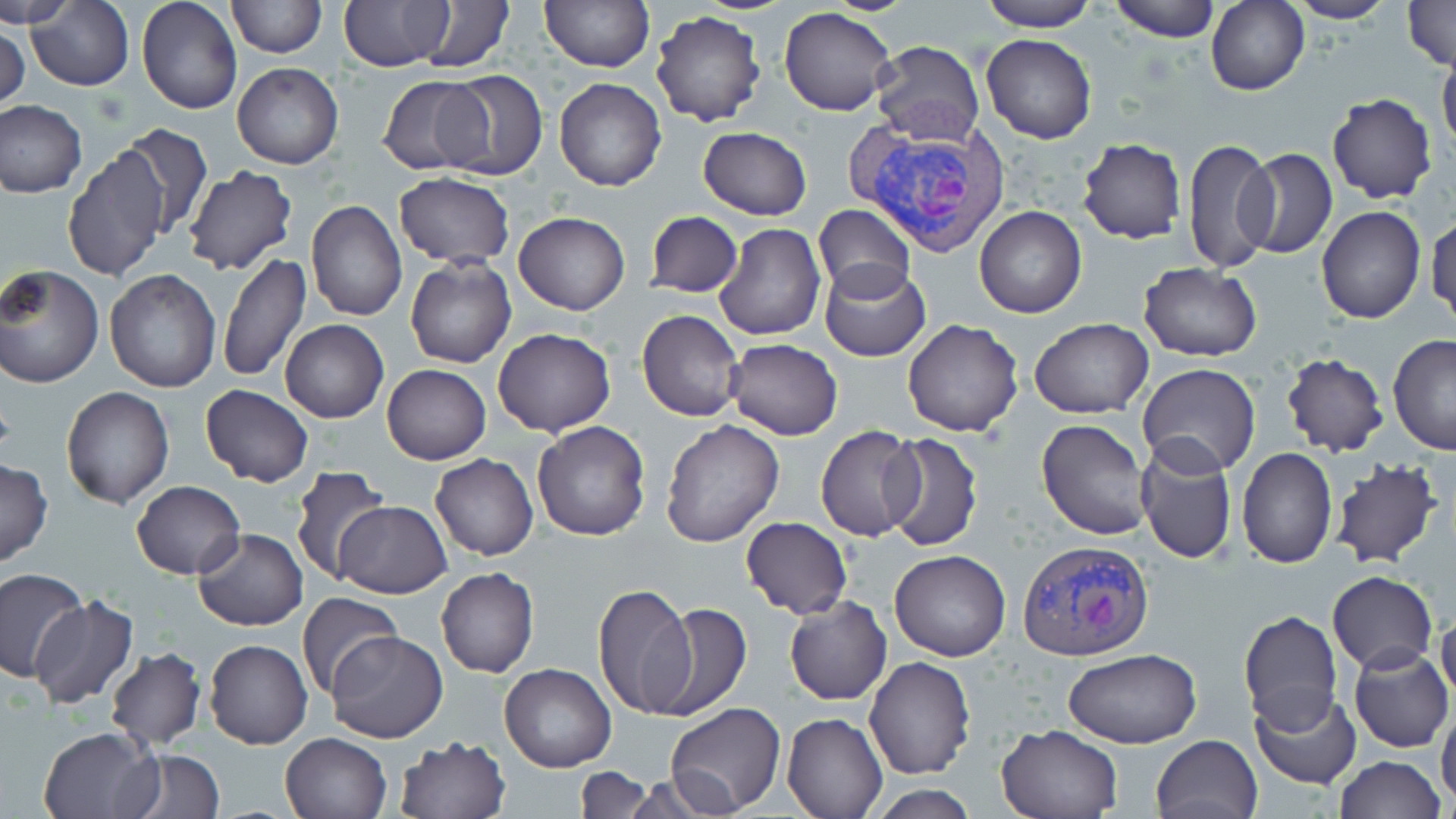
Approximate bounding boxes as (x1,y1)-(x2,y2) corner pairs in pixels. Plasmodium vivax-infected red blood cell locations: (834,96)-(1009,255), (1016,540)-(1155,662). Uninfected red blood cell locations: (4,0)-(76,28), (136,0)-(242,116), (225,0)-(325,57), (340,0)-(454,71), (414,0)-(515,72), (977,0)-(1098,32), (1110,0)-(1220,41), (1284,0)-(1397,24), (1402,0)-(1454,70), (540,1)-(654,72), (1206,1)-(1308,96), (27,2)-(134,92), (778,5)-(897,116), (650,11)-(768,127), (0,20)-(29,116), (981,34)-(1097,144), (871,39)-(985,146), (1438,49)-(1456,157), (232,63)-(343,168), (435,69)-(547,182), (378,75)-(490,176), (554,77)-(667,192), (1327,93)-(1436,205), (0,99)-(87,198), (112,123)-(211,240), (698,126)-(812,221), (1077,138)-(1186,244), (1182,138)-(1277,276), (63,142)-(170,283), (1238,147)-(1337,259), (182,165)-(299,277), (393,173)-(515,268), (306,200)-(406,320), (811,202)-(915,300), (974,205)-(1087,319), (1316,206)-(1426,325), (513,211)-(629,315), (646,211)-(743,298), (1427,212)-(1456,328), (715,222)-(826,342), (218,252)-(311,384), (405,256)-(516,369), (1138,262)-(1262,361), (819,264)-(930,360), (1,265)-(104,389), (103,269)-(222,392), (637,311)-(743,422), (902,318)-(1025,437), (1030,318)-(1151,419), (279,319)-(388,423), (492,327)-(616,437), (1388,332)-(1456,455), (724,338)-(842,440), (1280,354)-(1389,457), (382,364)-(491,464), (1136,365)-(1260,479), (200,385)-(314,488), (61,387)-(175,509), (1037,419)-(1152,540), (660,420)-(784,546), (531,421)-(652,540), (814,424)-(925,541), (879,432)-(983,549), (1134,440)-(1238,566), (1237,447)-(1337,568), (430,453)-(538,560), (0,458)-(53,568), (1328,458)-(1444,570), (290,465)-(392,583), (132,479)-(246,580), (334,499)-(453,598), (741,517)-(852,619), (193,528)-(307,632), (889,549)-(1011,661), (0,567)-(89,685), (436,568)-(539,678), (1327,572)-(1437,675), (592,582)-(697,719), (296,592)-(403,698), (27,596)-(138,708), (784,596)-(893,705), (1435,602)-(1456,706), (648,603)-(751,722), (1239,610)-(1342,730), (326,629)-(447,743), (205,640)-(313,749), (1349,646)-(1455,753), (1062,647)-(1202,748), (105,648)-(206,749), (864,656)-(976,778), (499,662)-(616,772), (1250,688)-(1359,790), (1436,700)-(1456,810), (665,702)-(785,816), (782,713)-(887,819), (997,723)-(1126,819), (38,726)-(160,819), (279,732)-(393,819), (1151,734)-(1262,819), (393,736)-(510,819), (117,748)-(224,818), (1334,755)-(1444,818), (574,766)-(656,819), (614,774)-(739,817), (870,783)-(978,818). Slide-level diagnosis: Plasmodium vivax. Optical microscopy. 1000x magnification. Thin blood film. Single field of view. Image is 1456×819 pixels. May-Grünwald-Giemsa-stained preparation.